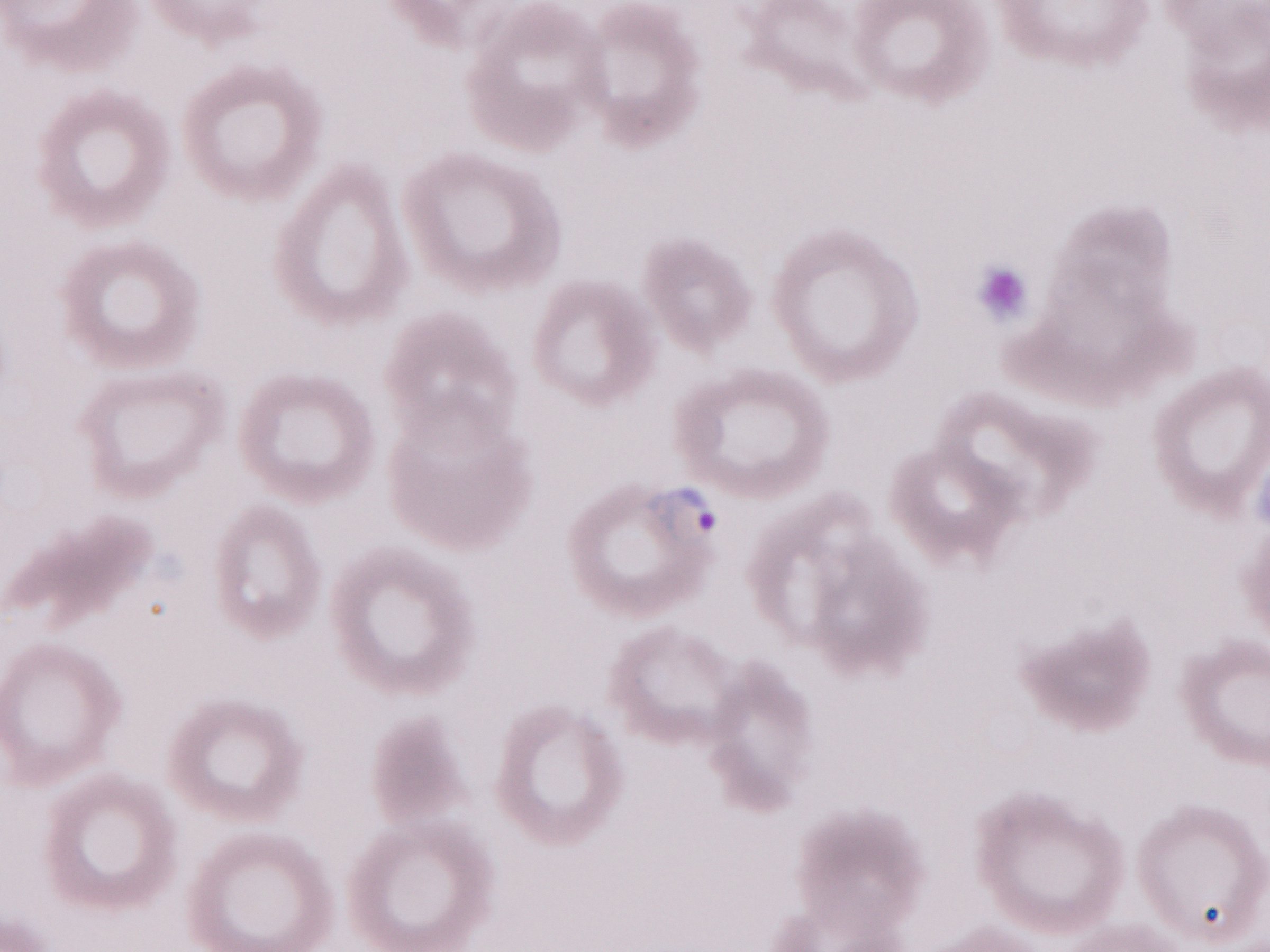 Magnification: 1,000x. May-Grünwald-Giemsa stain. Image is 1270×952 pixels. One field of this slide. Thin blood smear. Malaria diagnosis (patient-level): positive. Olympus BX43 microscope and DP73 digital camera.